Report the malaria status of this cell.
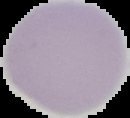
Uninfected.

Image is 130×118 pixels. Segmented cell region on a black background. From a thin blood film.